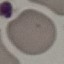

Summary:
  - Malaria status: uninfected
  - Capture: smartphone through the microscope eyepiece
  - Preparation: thin blood smear
  - Image type: cell patch, automatically extracted from a larger field of view and resized to 64 × 64 pixels
  - Stain: Giemsa